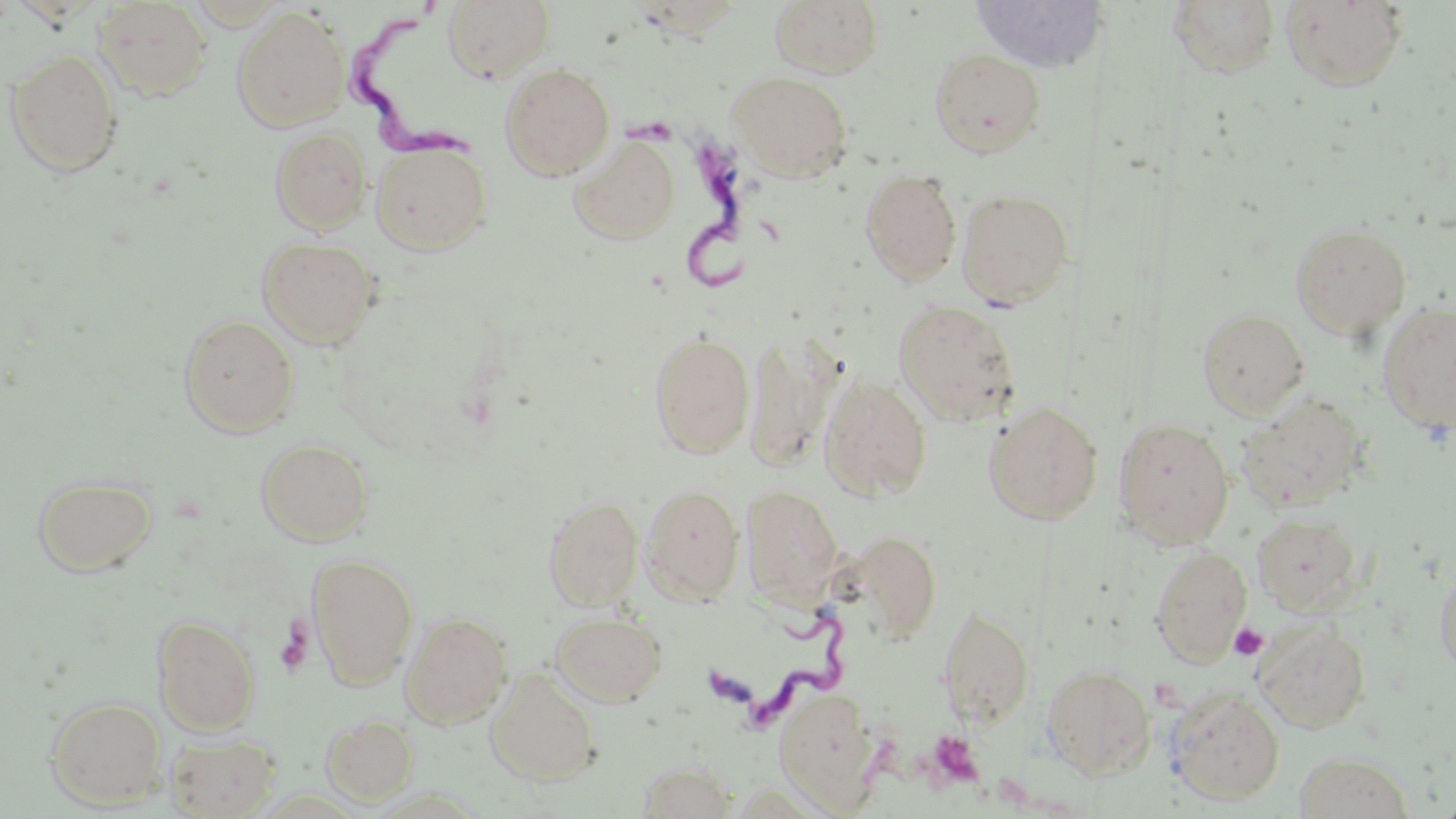

Approximate bounding boxes as named x1/y1/x2/y2 corners in pixels. Platelet locations: (x1=1229, y1=623, x2=1269, y2=660), (x1=925, y1=729, x2=983, y2=787). Trypanosoma brucei locations: (x1=340, y1=2, x2=487, y2=174), (x1=622, y1=106, x2=757, y2=296), (x1=702, y1=600, x2=851, y2=729). Uninfected red blood cell locations: (x1=770, y1=0, x2=883, y2=78), (x1=969, y1=0, x2=1098, y2=72), (x1=1280, y1=0, x2=1408, y2=91), (x1=92, y1=1, x2=212, y2=101), (x1=442, y1=1, x2=555, y2=82), (x1=1166, y1=1, x2=1282, y2=79), (x1=232, y1=7, x2=350, y2=131), (x1=929, y1=47, x2=1046, y2=157), (x1=5, y1=49, x2=123, y2=177), (x1=500, y1=63, x2=616, y2=179), (x1=727, y1=70, x2=854, y2=182), (x1=269, y1=128, x2=372, y2=233), (x1=569, y1=134, x2=680, y2=244), (x1=370, y1=139, x2=492, y2=255), (x1=860, y1=167, x2=962, y2=286), (x1=956, y1=188, x2=1073, y2=308), (x1=1290, y1=221, x2=1412, y2=339), (x1=257, y1=236, x2=380, y2=348), (x1=893, y1=299, x2=1021, y2=427), (x1=1376, y1=301, x2=1456, y2=433), (x1=1197, y1=307, x2=1309, y2=419), (x1=178, y1=313, x2=299, y2=436), (x1=648, y1=331, x2=755, y2=458), (x1=743, y1=334, x2=841, y2=471), (x1=819, y1=374, x2=932, y2=501), (x1=1237, y1=393, x2=1368, y2=513), (x1=983, y1=401, x2=1104, y2=524), (x1=1114, y1=416, x2=1235, y2=548), (x1=256, y1=438, x2=375, y2=546), (x1=32, y1=473, x2=157, y2=576), (x1=641, y1=483, x2=744, y2=605), (x1=741, y1=485, x2=844, y2=608), (x1=543, y1=494, x2=644, y2=610), (x1=1252, y1=512, x2=1362, y2=614), (x1=842, y1=530, x2=943, y2=643), (x1=1150, y1=546, x2=1252, y2=667), (x1=306, y1=552, x2=419, y2=689), (x1=1434, y1=562, x2=1456, y2=681), (x1=937, y1=603, x2=1035, y2=728), (x1=550, y1=610, x2=667, y2=706), (x1=400, y1=611, x2=513, y2=729), (x1=152, y1=614, x2=260, y2=735), (x1=1254, y1=619, x2=1371, y2=733), (x1=1042, y1=663, x2=1157, y2=777), (x1=486, y1=667, x2=602, y2=785), (x1=773, y1=686, x2=879, y2=810), (x1=1167, y1=688, x2=1285, y2=805), (x1=44, y1=694, x2=166, y2=809), (x1=321, y1=713, x2=419, y2=806), (x1=166, y1=733, x2=281, y2=818), (x1=1294, y1=751, x2=1413, y2=818), (x1=638, y1=760, x2=737, y2=818). Slide-level diagnosis: Trypanosoma brucei. One field of a larger specimen. Optical microscopy. May-Grünwald-Giemsa-stained preparation. 1000x magnification. Image is 1456×819 pixels. Thin blood smear.